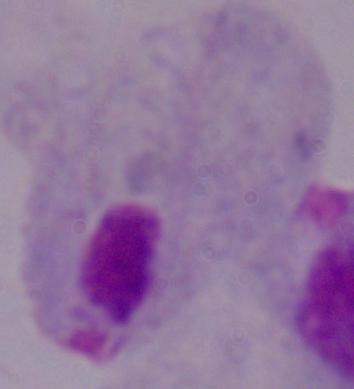

modality = micrograph
magnification = 1000x
identification = trichomonad